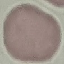

malaria status = uninfected
capture = smartphone through the microscope eyepiece
preparation = thin blood film
image type = automatically extracted cell patch, resized to 64 × 64 pixels
stain = Giemsa